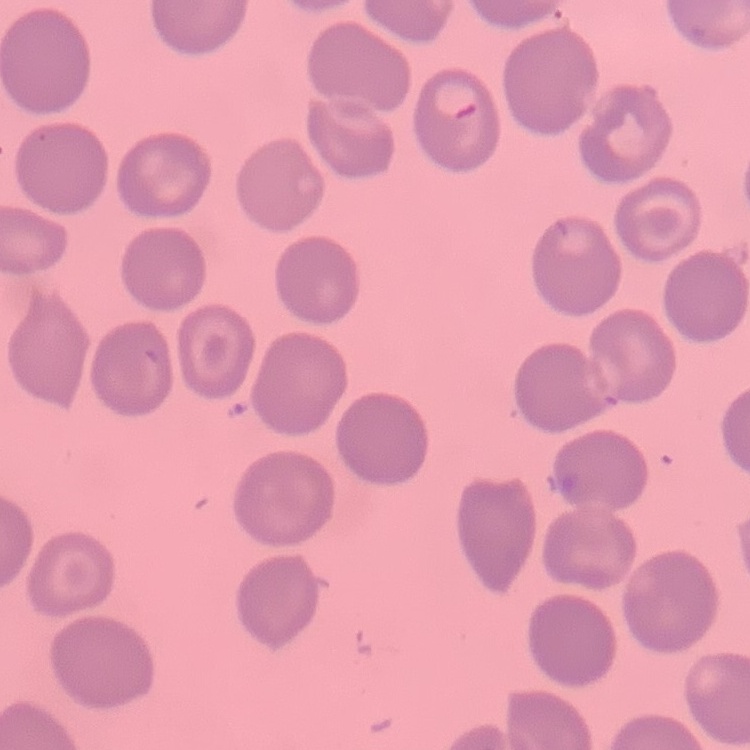

The red blood cells exhibit no rouleaux formation. Thin blood film. Square crop of a larger photomicrograph. Field's or Giemsa stain.